Identify the blood parasite species.
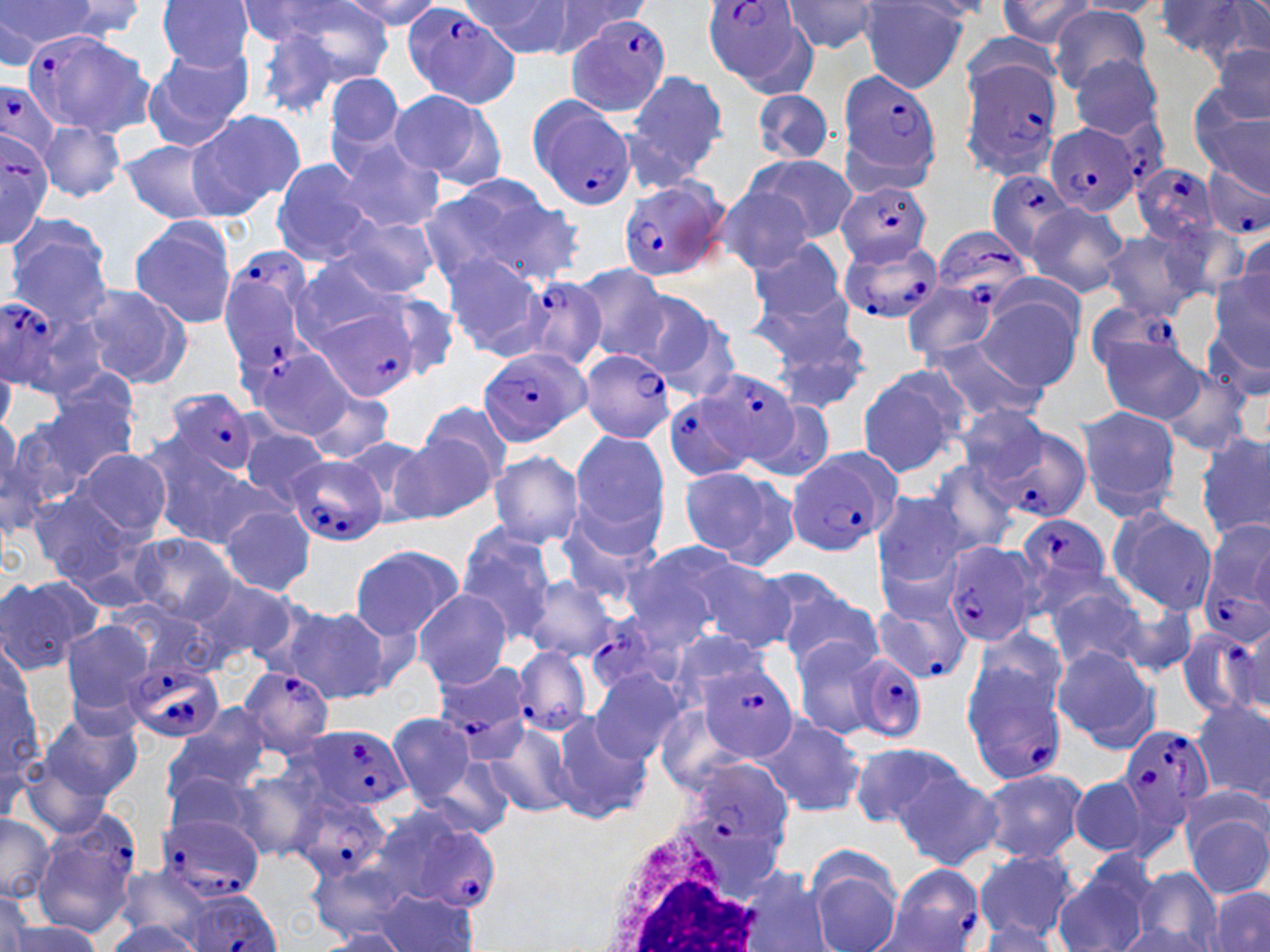
Plasmodium falciparum.

image size = 1270×952 pixels
magnification = 1000x
Plasmodium falciparum-infected red blood cell locations (subset) = approximate bounding boxes as [x1, y1, x2, y2] in pixels: [401, 1, 520, 107], [700, 2, 815, 91], [27, 24, 153, 139], [959, 58, 1064, 174], [835, 70, 941, 180], [0, 82, 62, 162], [526, 96, 635, 210], [1045, 123, 1139, 217], [0, 127, 54, 246], [1132, 164, 1222, 245], [1202, 165, 1270, 242], [985, 168, 1075, 258], [619, 178, 730, 279], [835, 182, 930, 265], [933, 226, 1034, 310], [838, 240, 944, 325], [218, 249, 317, 375], [514, 275, 606, 372], [1, 289, 86, 391], [1082, 300, 1193, 383], [318, 307, 420, 402], [238, 336, 357, 439], [477, 346, 590, 447], [577, 347, 676, 443], [692, 368, 803, 469], [165, 387, 260, 480], [663, 389, 759, 481], [994, 431, 1091, 522], [787, 449, 899, 554], [286, 452, 390, 548], [1016, 511, 1115, 601], [941, 542, 1035, 647], [1200, 563, 1270, 641], [868, 594, 972, 687], [584, 606, 655, 689], [1177, 630, 1261, 722], [513, 645, 594, 738], [845, 652, 929, 742], [126, 658, 226, 743], [699, 658, 799, 760], [430, 662, 534, 756], [239, 665, 335, 757], [960, 691, 1070, 784], [1114, 722, 1216, 830], [298, 725, 411, 813], [676, 757, 796, 871], [291, 795, 392, 880], [368, 805, 501, 918], [31, 813, 141, 938], [156, 814, 265, 900], [880, 865, 986, 952]
uninfected red blood cell locations (subset) = approximate bounding boxes as [x1, y1, x2, y2] in pixels: [1, 0, 99, 56], [155, 0, 256, 72], [338, 0, 442, 31], [539, 0, 647, 53], [995, 0, 1099, 48], [48, 1, 151, 40], [237, 1, 364, 47], [264, 1, 395, 89], [464, 1, 575, 56], [781, 1, 888, 55], [858, 1, 968, 92], [1072, 1, 1171, 17], [1152, 2, 1262, 64], [1049, 5, 1152, 91], [247, 23, 356, 121], [1208, 41, 1270, 128], [140, 48, 253, 150], [1068, 54, 1165, 140], [325, 71, 405, 153], [625, 71, 729, 174], [750, 88, 838, 164], [386, 89, 499, 184], [1194, 97, 1270, 195], [185, 110, 304, 218], [38, 120, 125, 203], [328, 135, 445, 233], [120, 139, 229, 223], [744, 154, 858, 243], [269, 159, 380, 267], [421, 174, 581, 289], [712, 183, 814, 274], [1027, 204, 1130, 299], [6, 216, 118, 326], [331, 217, 441, 298], [129, 218, 238, 328], [1153, 218, 1247, 305], [1100, 231, 1203, 323], [1232, 231, 1269, 316], [746, 236, 849, 326], [442, 253, 549, 358], [290, 256, 412, 344], [570, 263, 670, 361], [1207, 275, 1270, 390], [75, 283, 194, 390], [903, 283, 999, 359], [632, 287, 738, 397], [753, 288, 868, 409], [376, 290, 463, 381], [975, 295, 1080, 390], [1096, 333, 1207, 424], [924, 339, 1048, 425], [1151, 363, 1254, 456], [856, 367, 967, 477], [30, 380, 137, 481], [304, 386, 397, 464], [740, 393, 836, 485], [419, 400, 512, 491], [952, 404, 1055, 489], [1075, 406, 1181, 520], [0, 418, 67, 530], [241, 424, 333, 509], [1197, 430, 1269, 544], [391, 431, 495, 522], [569, 431, 669, 547], [339, 434, 445, 523], [147, 441, 267, 550], [69, 446, 172, 544], [487, 449, 584, 549], [924, 460, 1021, 558], [676, 466, 786, 562], [24, 490, 138, 582], [872, 493, 966, 599], [219, 504, 316, 597], [1107, 507, 1217, 615], [558, 522, 660, 609], [454, 529, 558, 642], [128, 533, 238, 623], [619, 541, 752, 649], [348, 543, 465, 640], [683, 560, 796, 653], [724, 562, 842, 655], [0, 574, 100, 675], [186, 574, 302, 669], [523, 575, 617, 661], [770, 582, 882, 675], [1044, 588, 1152, 670], [411, 589, 512, 689], [1111, 600, 1199, 679], [276, 604, 392, 703], [59, 619, 158, 716], [665, 628, 776, 715], [970, 629, 1071, 719], [788, 636, 889, 742], [1049, 644, 1161, 752], [1, 661, 45, 782], [589, 669, 687, 764], [1191, 696, 1270, 802], [167, 707, 275, 802], [39, 709, 142, 802], [548, 709, 652, 825], [386, 713, 477, 807], [757, 713, 865, 818], [479, 718, 580, 819], [850, 741, 967, 834], [228, 766, 334, 861], [163, 767, 265, 845], [979, 768, 1085, 864], [894, 770, 1003, 869], [1072, 776, 1151, 858], [1186, 812, 1270, 900], [0, 813, 56, 904], [973, 849, 1078, 944], [808, 854, 903, 952], [1054, 863, 1152, 952], [1130, 867, 1226, 952], [735, 870, 832, 952], [110, 881, 211, 952], [1205, 888, 1270, 952], [0, 891, 33, 952], [369, 892, 486, 952], [105, 918, 201, 952], [976, 918, 1065, 949], [3, 921, 104, 951], [1117, 925, 1213, 951], [320, 929, 411, 951]
field of view = single
stain = May-Grünwald-Giemsa
white blood cell locations = approximate bounding boxes as [x1, y1, x2, y2] in pixels: [593, 832, 777, 952]
preparation = thin blood film
modality = optical microscopy